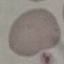
result = no malaria parasites seen
capture = smartphone camera at the microscope eyepiece
stain = Giemsa
preparation = thin blood smear
image type = automatically extracted cell patch, resized to 64 × 64 pixels